Find the cells and give the type of each one.
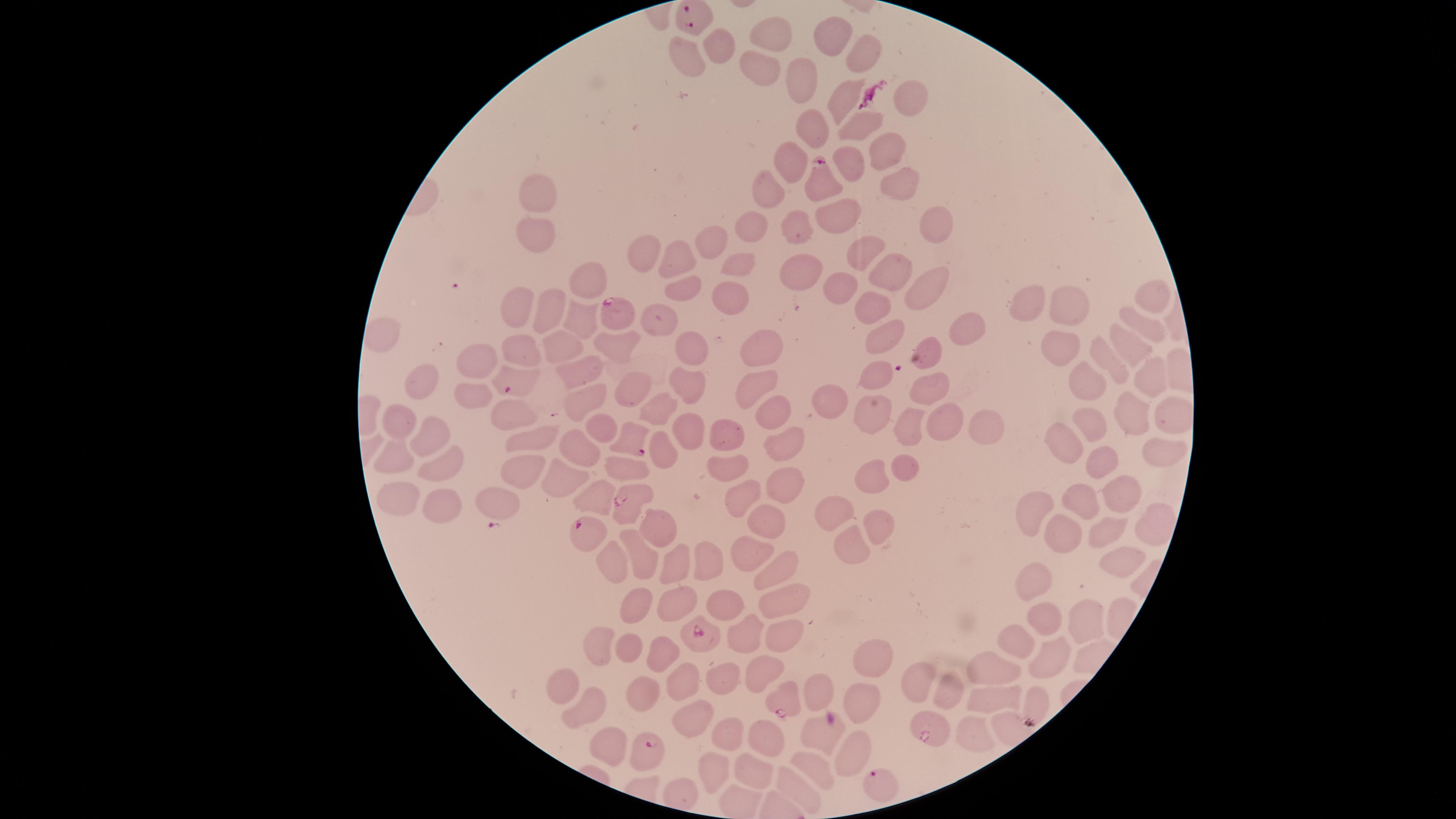

Approximate marker points, in pixels from the top-left corner.
Parasitized RBCs: (x=690, y=18), (x=820, y=182), (x=619, y=310), (x=514, y=381), (x=629, y=438), (x=623, y=505), (x=592, y=528), (x=695, y=631), (x=783, y=698), (x=928, y=733), (x=645, y=752), (x=880, y=784).
Uninfected RBCs: (x=767, y=33), (x=831, y=36), (x=716, y=46), (x=866, y=52), (x=686, y=60), (x=755, y=68), (x=801, y=72), (x=901, y=93), (x=834, y=98), (x=815, y=128), (x=863, y=128), (x=883, y=152), (x=850, y=158), (x=794, y=160), (x=766, y=190), (x=899, y=191), (x=539, y=193), (x=937, y=217), (x=834, y=221), (x=755, y=225), (x=802, y=227), (x=536, y=236), (x=714, y=244), (x=855, y=249), (x=644, y=256), (x=741, y=261), (x=677, y=263), (x=588, y=270), (x=892, y=270), (x=794, y=274), (x=835, y=282), (x=683, y=287), (x=928, y=288), (x=1155, y=292), (x=734, y=296), (x=871, y=303), (x=518, y=307), (x=1032, y=307), (x=1068, y=307), (x=548, y=311), (x=579, y=320), (x=660, y=320), (x=959, y=321), (x=1142, y=322), (x=882, y=331), (x=383, y=337), (x=758, y=337), (x=688, y=344), (x=1129, y=344), (x=612, y=346), (x=1060, y=347), (x=559, y=348), (x=927, y=349), (x=517, y=350), (x=1106, y=362), (x=480, y=366), (x=585, y=372), (x=685, y=379), (x=882, y=380), (x=1143, y=380), (x=422, y=383), (x=755, y=383), (x=628, y=384), (x=1084, y=384), (x=931, y=386), (x=472, y=393), (x=584, y=395), (x=830, y=401), (x=662, y=406), (x=774, y=408), (x=513, y=415), (x=872, y=415), (x=1135, y=416), (x=948, y=419), (x=397, y=422), (x=981, y=423), (x=909, y=426), (x=600, y=427), (x=1088, y=428), (x=681, y=433), (x=728, y=435), (x=534, y=437), (x=434, y=442), (x=784, y=442), (x=1064, y=442), (x=657, y=451), (x=1157, y=452), (x=577, y=453), (x=395, y=456), (x=1098, y=458), (x=615, y=467), (x=724, y=467), (x=516, y=468), (x=908, y=470), (x=447, y=471), (x=563, y=472), (x=880, y=476), (x=771, y=489), (x=1121, y=493), (x=492, y=495), (x=591, y=495), (x=745, y=495), (x=397, y=499), (x=1087, y=506), (x=1029, y=509), (x=441, y=511), (x=830, y=512), (x=763, y=517), (x=876, y=522), (x=1143, y=522), (x=650, y=524), (x=1103, y=530), (x=1051, y=537), (x=844, y=544), (x=744, y=546), (x=639, y=554), (x=612, y=556), (x=715, y=564), (x=674, y=566), (x=1108, y=566), (x=777, y=568), (x=1035, y=576), (x=775, y=600), (x=671, y=601), (x=633, y=602), (x=729, y=607), (x=1076, y=618), (x=1042, y=620), (x=745, y=635), (x=780, y=635), (x=598, y=637), (x=1013, y=639), (x=620, y=646), (x=1048, y=654), (x=656, y=655), (x=874, y=659), (x=997, y=667), (x=758, y=670), (x=726, y=678), (x=921, y=680), (x=679, y=685), (x=568, y=688), (x=951, y=693), (x=819, y=694), (x=636, y=696), (x=993, y=696), (x=1037, y=701), (x=852, y=704), (x=588, y=707), (x=694, y=714), (x=728, y=726), (x=972, y=729), (x=757, y=742), (x=610, y=746), (x=845, y=755), (x=810, y=763), (x=715, y=771), (x=757, y=775), (x=797, y=788).
No WBCs identified.

{
  "image_size": "1456×819 pixels",
  "capture": "smartphone photograph through the microscope eyepiece",
  "visible_region": "circular",
  "species": "Plasmodium falciparum",
  "field_of_view": "single",
  "preparation": "thin blood film",
  "stain": "Giemsa"
}